Identify the parasite.
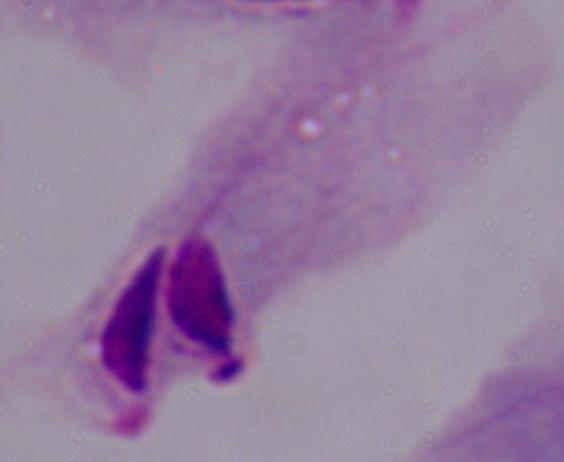
A trichomonad.

Captured at 1000x magnification. Photomicrograph.